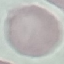
Result: no malaria parasites detected. Photographed with a smartphone camera at the microscope eyepiece. Cell patch, automatically extracted from a larger field of view and resized to 64 × 64 pixels. Thin smear of blood. Giemsa stain.